Assess this cell for malaria.
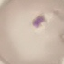

Parasitized.

Summary:
  - Capture: smartphone through the microscope eyepiece
  - Image type: automatically extracted cell patch, resized to 64 × 64 pixels
  - Stain: Giemsa
  - Preparation: thin blood film